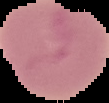 Image is 109×103 pixels. The area outside the segmented cell region is set to black. Malaria status: uninfected. From a thin blood film.